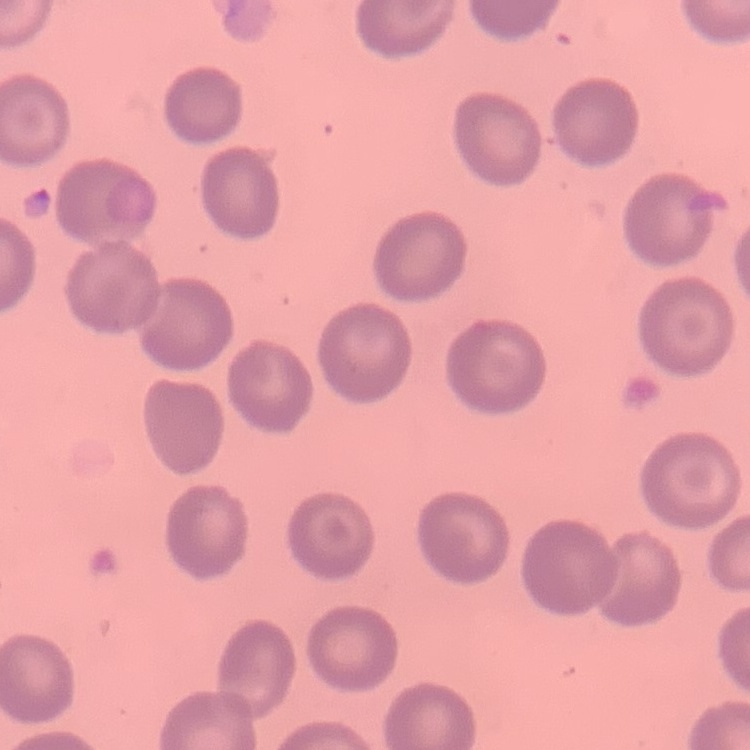
Summary:
  - Erythrocyte morphology: no rouleaux formation
  - Image type: one tile cut from a larger photomicrograph
  - Preparation: thin blood film
  - Stain: Field's or Giemsa